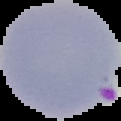
Summary:
  - Preparation: thin blood film
  - Result: malaria parasites identified
  - Image type: cell region segmented out of the field of view; surrounding area masked to black
  - Image size: 121×121 pixels